Identify the blood parasite species.
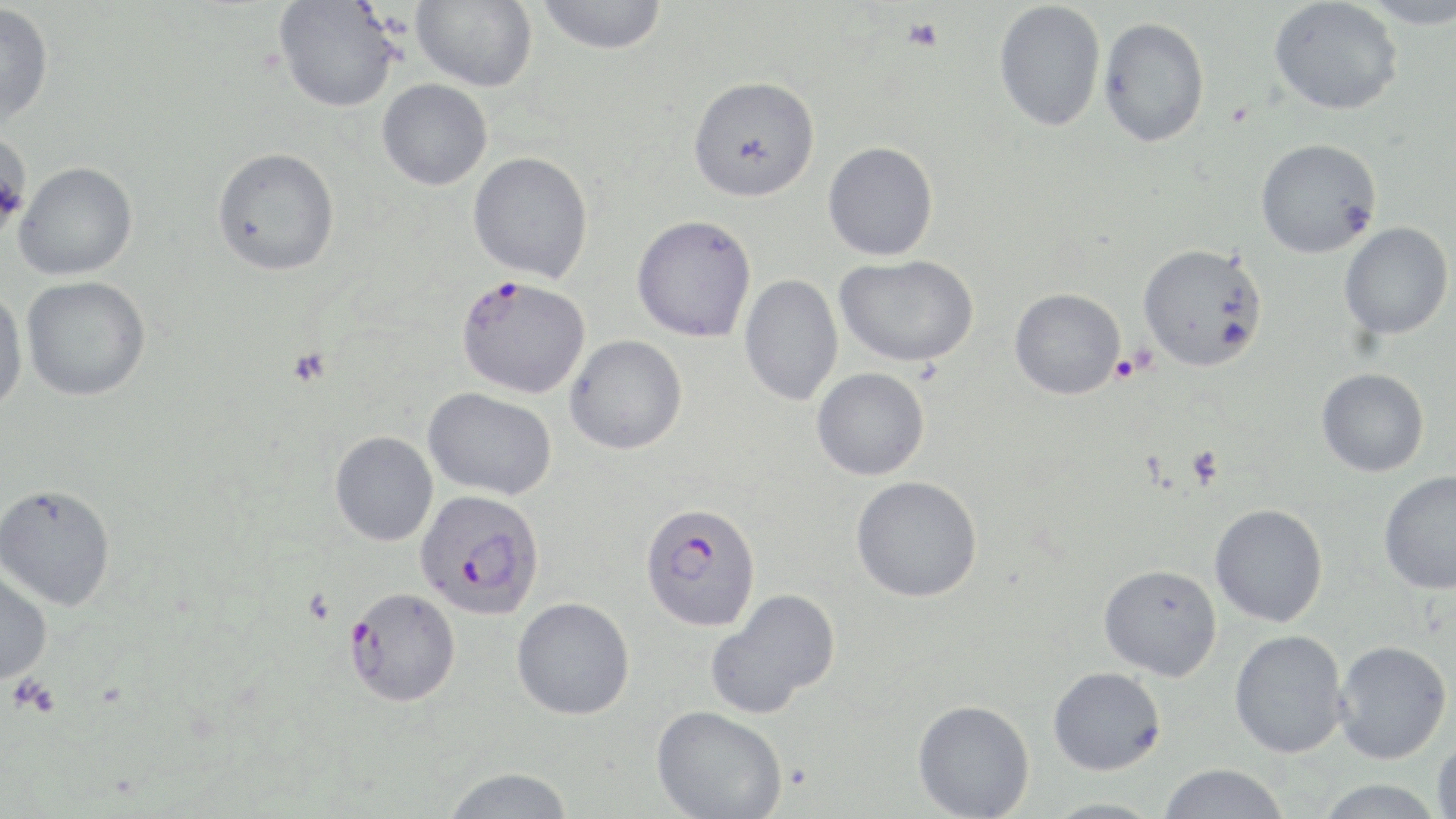
Plasmodium falciparum.

{
  "stain": "May-Grünwald-Giemsa",
  "image_size": "1456×819 pixels",
  "uninfected_red_blood_cell_locations": "approximate bounding boxes as named x1/y1/x2/y2 corners in pixels: (x1=411, y1=0, x2=537, y2=93), (x1=536, y1=0, x2=668, y2=54), (x1=1268, y1=0, x2=1403, y2=115), (x1=1357, y1=0, x2=1456, y2=28), (x1=274, y1=1, x2=401, y2=113), (x1=993, y1=1, x2=1106, y2=132), (x1=0, y1=3, x2=54, y2=126), (x1=1098, y1=16, x2=1210, y2=148), (x1=688, y1=75, x2=820, y2=202), (x1=377, y1=79, x2=492, y2=190), (x1=0, y1=128, x2=32, y2=247), (x1=1255, y1=138, x2=1381, y2=258), (x1=822, y1=142, x2=938, y2=261), (x1=212, y1=147, x2=340, y2=276), (x1=468, y1=151, x2=594, y2=283), (x1=14, y1=162, x2=138, y2=281), (x1=631, y1=214, x2=756, y2=342), (x1=1339, y1=222, x2=1453, y2=340), (x1=1137, y1=243, x2=1268, y2=372), (x1=834, y1=254, x2=979, y2=367), (x1=739, y1=274, x2=843, y2=406), (x1=21, y1=276, x2=150, y2=401), (x1=0, y1=287, x2=28, y2=419), (x1=1009, y1=288, x2=1126, y2=399), (x1=565, y1=334, x2=687, y2=455), (x1=811, y1=367, x2=930, y2=480), (x1=1317, y1=368, x2=1429, y2=477), (x1=423, y1=387, x2=557, y2=500), (x1=330, y1=431, x2=438, y2=546), (x1=1379, y1=470, x2=1456, y2=594), (x1=851, y1=476, x2=982, y2=602), (x1=1, y1=483, x2=116, y2=611), (x1=1210, y1=504, x2=1328, y2=627), (x1=1098, y1=564, x2=1222, y2=681), (x1=0, y1=566, x2=52, y2=685), (x1=705, y1=588, x2=841, y2=719), (x1=512, y1=597, x2=635, y2=719), (x1=1229, y1=629, x2=1348, y2=758), (x1=1333, y1=640, x2=1452, y2=764), (x1=1048, y1=666, x2=1166, y2=775), (x1=912, y1=699, x2=1035, y2=819), (x1=651, y1=705, x2=788, y2=819), (x1=1433, y1=735, x2=1456, y2=819), (x1=1157, y1=763, x2=1290, y2=819), (x1=441, y1=767, x2=575, y2=819), (x1=1314, y1=779, x2=1446, y2=819), (x1=1043, y1=798, x2=1164, y2=818)",
  "field_of_view": "single",
  "magnification": "1000x",
  "modality": "light microscopy",
  "plasmodium_falciparum_infected_red_blood_cell_locations": "approximate bounding boxes as named x1/y1/x2/y2 corners in pixels: (x1=455, y1=274, x2=590, y2=399), (x1=415, y1=488, x2=546, y2=619), (x1=639, y1=502, x2=762, y2=632), (x1=345, y1=587, x2=460, y2=707)",
  "platelet_locations": "approximate bounding boxes as named x1/y1/x2/y2 corners in pixels: (x1=902, y1=17, x2=944, y2=53), (x1=1109, y1=354, x2=1143, y2=383), (x1=1187, y1=446, x2=1223, y2=487), (x1=9, y1=674, x2=59, y2=718)",
  "preparation": "thin blood film"
}